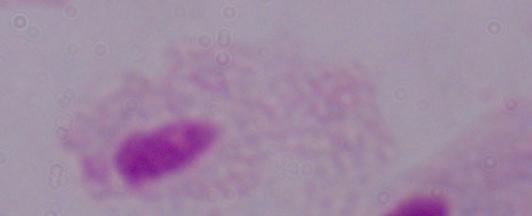

Summary:
  - Identification: trichomonad
  - Magnification: 1000x
  - Modality: photomicrograph